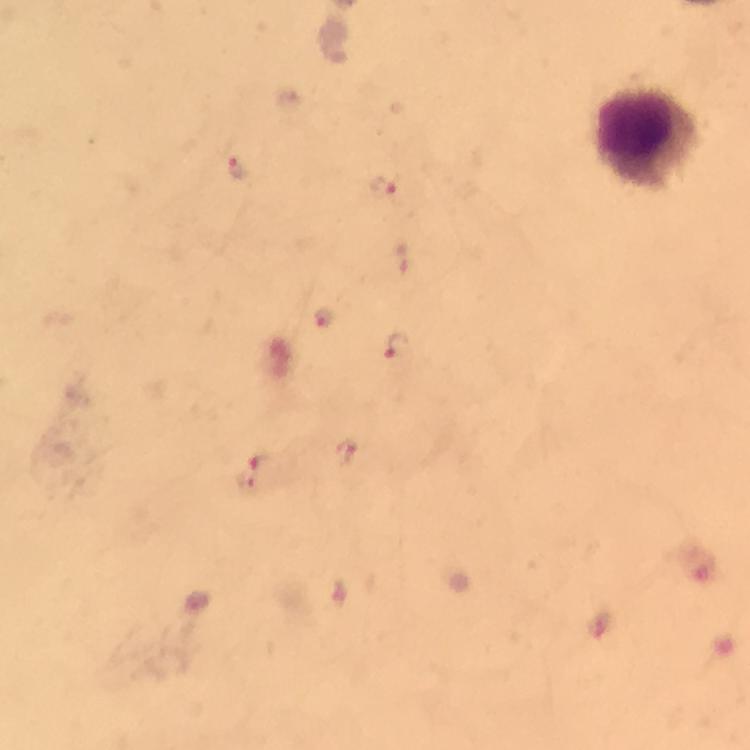
Approximate centers as (x, y) in pixels.
Summary:
  - Plasmodium parasite locations: (235, 169), (383, 186), (323, 319), (397, 347), (345, 453), (260, 462), (243, 483)
  - Leukocyte locations: (647, 141)
  - Immersion oil: used
  - Capture: smartphone camera through the microscope
  - Image size: 750×750 pixels
  - Magnification: 100x
  - Preparation: thick blood smear
  - Context: from a malaria diagnostic workup
  - Stain: Giemsa
  - Cropped from: one field of view